Describe the morphology of the red blood cells.
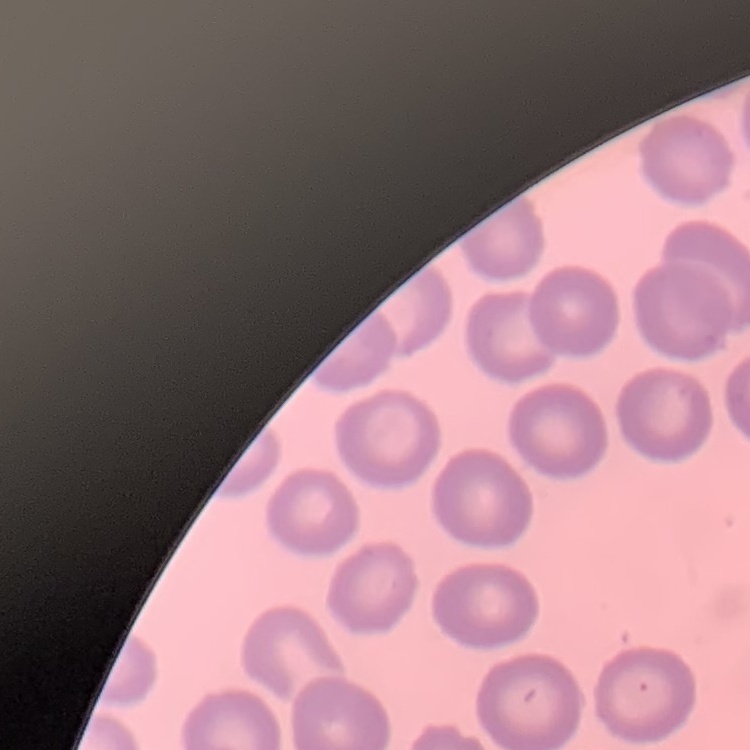

No rouleaux formation.

Summary:
  - Preparation: thin blood smear
  - Image type: one tile cut from a larger photomicrograph
  - Stain: Field's or Giemsa